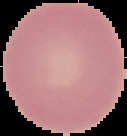
Summary:
  - Result: negative for malaria parasites
  - Preparation: thin blood film
  - Image size: 127×136 pixels
  - Image type: cell region segmented out of the field of view; surrounding area masked to black